Locate every Plasmodium falciparum-infected red blood cell.
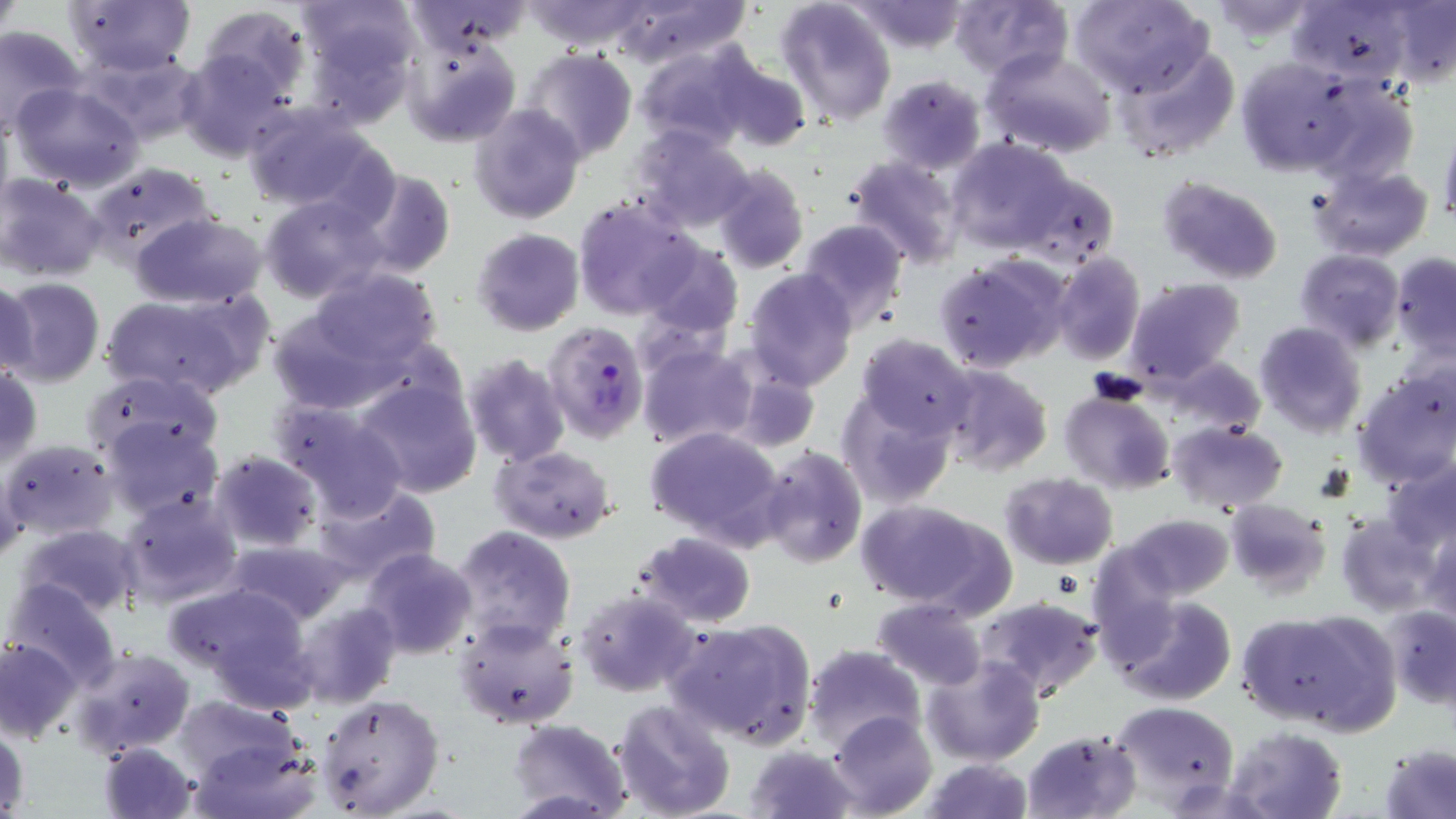

Approximate bounding boxes as [x1, y1, x2, y2] in pixels.
Plasmodium falciparum-infected red blood cells: [543, 320, 648, 443].

Uninfected red blood cell locations: [1, 0, 23, 43], [64, 0, 196, 74], [300, 0, 417, 96], [524, 0, 650, 51], [614, 0, 747, 67], [1072, 0, 1215, 100], [405, 1, 535, 55], [775, 1, 899, 127], [853, 1, 968, 53], [951, 1, 1071, 81], [1289, 1, 1420, 88], [1208, 3, 1321, 40], [1375, 3, 1456, 88], [195, 5, 311, 103], [0, 24, 87, 137], [403, 33, 521, 148], [634, 42, 756, 151], [1115, 45, 1240, 164], [980, 47, 1116, 161], [177, 48, 296, 162], [77, 49, 208, 147], [521, 49, 638, 162], [1235, 57, 1355, 174], [712, 58, 812, 152], [877, 74, 987, 175], [1306, 76, 1418, 184], [10, 83, 146, 191], [469, 103, 586, 224], [240, 106, 386, 215], [628, 124, 756, 232], [1438, 125, 1456, 227], [944, 137, 1081, 256], [846, 156, 965, 270], [712, 162, 809, 275], [89, 163, 216, 265], [1309, 164, 1432, 262], [1014, 166, 1118, 262], [351, 167, 456, 280], [0, 174, 107, 281], [1157, 176, 1283, 283], [258, 195, 388, 305], [571, 197, 699, 318], [130, 213, 269, 308], [795, 218, 909, 332], [472, 228, 584, 336], [635, 239, 743, 340], [1295, 249, 1404, 353], [1051, 252, 1145, 365], [1390, 252, 1456, 359], [934, 256, 1068, 374], [302, 268, 444, 370], [743, 268, 858, 391], [0, 276, 37, 385], [0, 278, 104, 387], [1124, 278, 1244, 388], [104, 289, 265, 403], [266, 295, 432, 415], [1254, 322, 1367, 437], [857, 333, 979, 442], [637, 342, 757, 450], [461, 353, 572, 467], [1163, 355, 1267, 438], [934, 364, 1053, 477], [0, 365, 42, 470], [729, 367, 820, 454], [1352, 367, 1456, 488], [83, 369, 225, 471], [354, 379, 484, 500], [835, 387, 959, 509], [1060, 390, 1175, 494], [270, 399, 410, 521], [102, 417, 222, 520], [1166, 419, 1288, 513], [645, 425, 785, 548], [1, 438, 120, 540], [489, 444, 617, 544], [757, 445, 867, 568], [209, 450, 321, 551], [1385, 456, 1456, 553], [0, 460, 25, 562], [999, 472, 1119, 569], [310, 485, 440, 588], [119, 491, 242, 609], [853, 498, 1012, 616], [1224, 499, 1333, 596], [1334, 512, 1444, 616], [1122, 514, 1234, 602], [448, 523, 578, 650], [20, 524, 143, 618], [1422, 526, 1456, 626], [634, 531, 758, 628], [225, 538, 353, 627], [1086, 543, 1183, 659], [363, 548, 478, 660], [5, 578, 121, 690], [164, 581, 316, 702], [575, 586, 699, 696], [1113, 594, 1235, 705], [977, 595, 1102, 700], [872, 598, 988, 690], [291, 599, 399, 710], [1383, 604, 1456, 707], [1241, 608, 1394, 734], [453, 615, 580, 731], [672, 619, 815, 750], [0, 635, 82, 743], [804, 645, 925, 753], [72, 647, 196, 758], [923, 655, 1043, 767], [316, 693, 443, 817], [171, 694, 304, 786], [612, 700, 736, 819], [1110, 701, 1239, 808], [827, 709, 938, 818], [508, 717, 630, 818], [1, 725, 29, 816], [1224, 726, 1348, 819], [1021, 729, 1140, 818], [187, 735, 321, 819], [98, 741, 199, 819], [746, 742, 859, 819], [1377, 742, 1455, 819], [920, 758, 1032, 818]. Slide-level diagnosis: Plasmodium falciparum. One field of a larger specimen. May-Grünwald-Giemsa-stained preparation. 1000x magnification. Thin blood film. Light microscopy. Image is 1456×819 pixels.